Describe the morphology of the red blood cells.
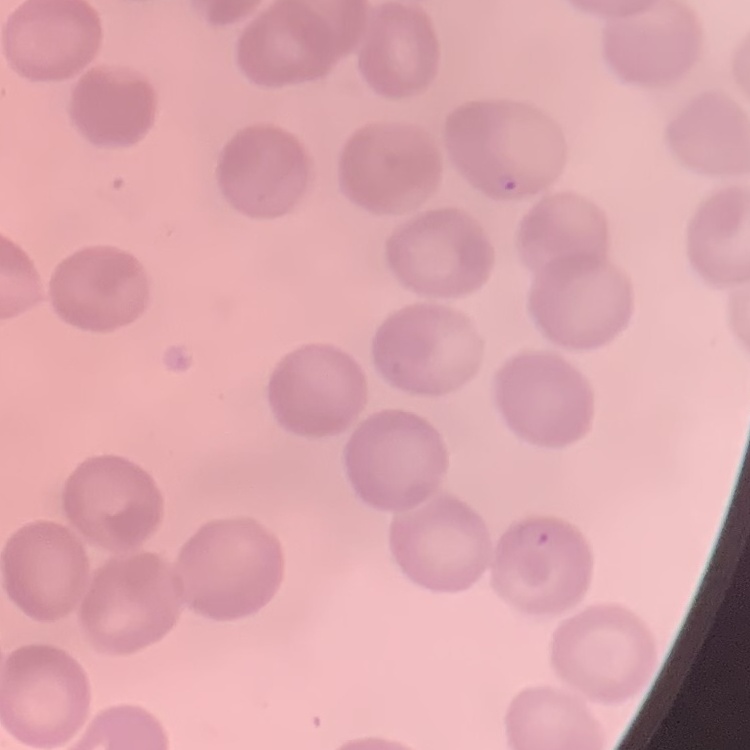
No rouleaux formation.

Summary:
  - Image type: one tile cut from a larger photomicrograph
  - Preparation: thin blood film
  - Stain: Field's or Giemsa